Report the malaria status of this cell.
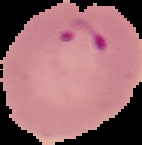

Parasitized.

Image is 142×145 pixels. From a thin blood smear. Cell region segmented out of the field of view; the surrounding area is masked to black.